Report the malaria status of this cell.
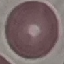

Uninfected.

Summary:
  - Preparation: thin smear
  - Stain: Giemsa
  - Image type: cell patch, automatically extracted from a larger field of view and resized to 64 × 64 pixels
  - Capture: smartphone through the microscope eyepiece